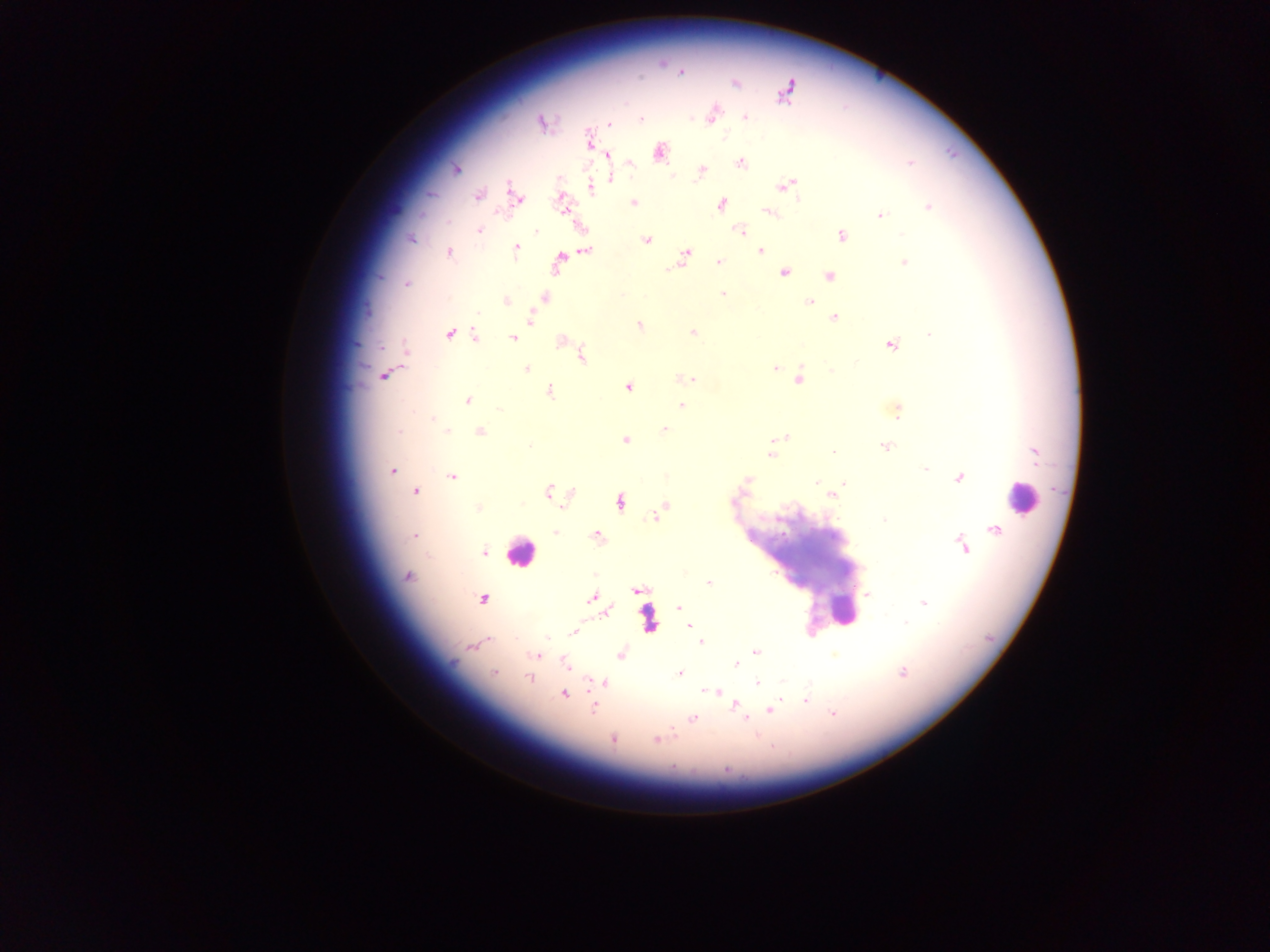

Approximate centers as x y in pixels.
Summary:
  - Leukocyte locations: 1022 497; 519 553; 844 609
  - Plasmodium parasite locations: 681 72; 735 83; 786 93; 712 117; 745 118; 641 119; 541 122; 609 124; 658 152; 607 155; 741 163; 910 163; 630 164; 456 169; 701 170; 671 176; 610 177; 788 185; 591 187; 479 196; 515 196; 561 201; 633 203; 721 204; 928 207; 770 212; 880 215; 478 230; 537 230; 739 230; 841 235; 411 238; 647 240; 516 249; 585 251; 760 251; 685 252; 450 253; 719 262; 558 263; 904 263; 668 269; 784 273; 829 276; 407 284; 723 293; 544 297; 506 300; 809 302; 531 317; 834 317; 639 326; 693 333; 449 334; 929 334; 476 336; 513 338; 561 340; 891 345; 582 356; 775 367; 527 369; 832 370; 384 375; 682 378; 690 379; 798 379; 628 387; 550 392; 468 401; 681 405; 897 411; 433 417; 665 429; 448 430; 399 431; 481 431; 780 437; 625 440; 529 446; 886 446; 833 452; 1035 453; 772 454; 925 468; 392 469; 452 477; 959 478; 746 480; 816 482; 844 483; 416 491; 549 491; 570 495; 831 495; 620 502; 663 507; 478 508; 655 516; 884 520; 995 529; 555 531; 597 536; 414 537; 963 547; 484 552; 407 576; 708 582; 637 590; 868 595; 592 598; 483 599; 597 603; 923 603; 679 607; 606 611; 905 622; 689 626; 573 633; 547 637; 700 642; 471 646; 757 652; 620 654; 535 656; 565 664; 736 665; 903 672; 493 673; 679 674; 528 678; 604 682; 757 684; 704 691; 716 691; 564 695; 806 700; 735 704; 594 708; 770 710; 833 714; 693 719; 746 719; 673 732; 612 739; 657 740; 673 768; 726 769
  - Preparation: thick blood smear
  - Image size: 1270×952 pixels
  - Capture: mobile-phone photograph through a microscope
  - Field of view: single
  - Country: Ghana